Locate every malaria parasite.
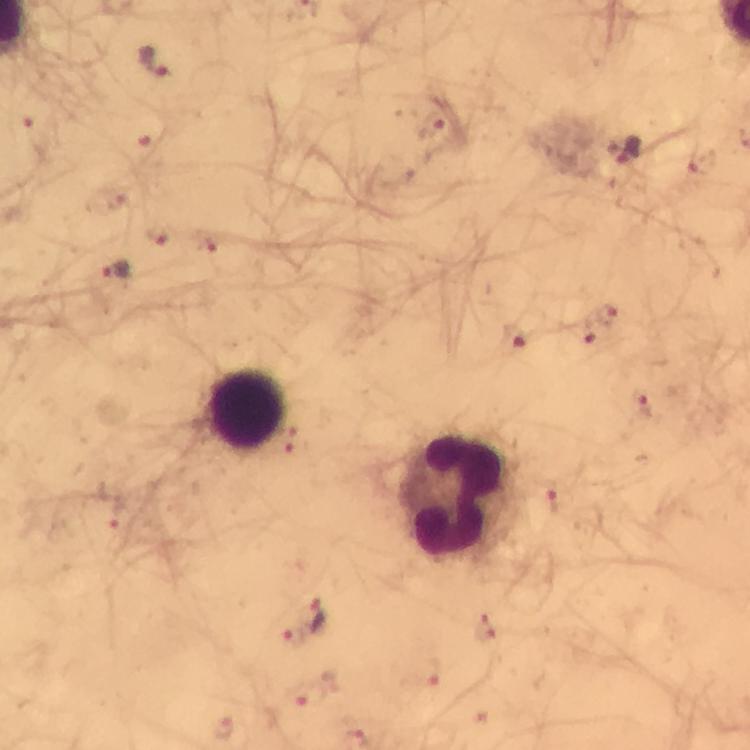

Approximate object centers, in pixels from the top-left corner.
Malaria parasites: (x=152, y=62), (x=430, y=125), (x=31, y=130), (x=147, y=147), (x=628, y=154), (x=699, y=162), (x=157, y=236), (x=207, y=243), (x=114, y=271), (x=605, y=314), (x=581, y=336), (x=516, y=339), (x=645, y=402), (x=286, y=440), (x=557, y=501), (x=116, y=513), (x=321, y=612), (x=486, y=629), (x=291, y=633), (x=429, y=675), (x=305, y=695), (x=220, y=727).

Leukocyte locations: (x=245, y=410), (x=461, y=499). A crop from one field of view. 100x magnification. Thick blood smear. Immersion oil was used. Giemsa stain. Photographed through the microscope with a smartphone camera. Image is 750×750 pixels. From a malaria diagnostic workup.